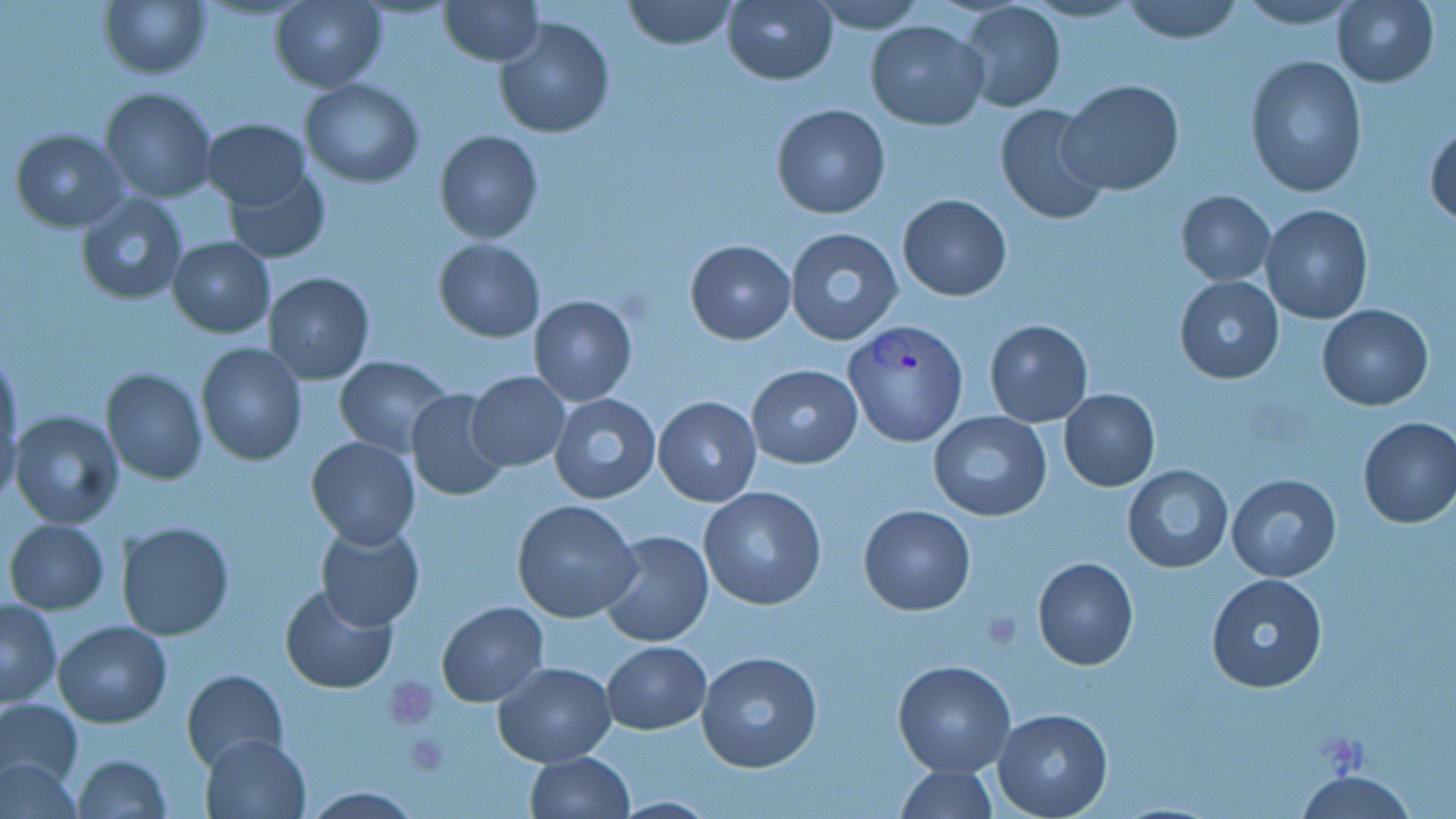

{
  "slide_level_diagnosis": "Plasmodium vivax",
  "preparation": "thin blood smear",
  "uninfected_red_blood_cell_locations": "approximate bounding boxes as [x1, y1, x2, y2] in pixels: [99, 0, 210, 79], [268, 0, 387, 91], [440, 0, 543, 66], [621, 0, 739, 50], [721, 0, 839, 85], [809, 0, 925, 31], [1121, 0, 1243, 44], [1234, 0, 1365, 28], [1333, 0, 1440, 86], [957, 2, 1066, 113], [494, 18, 616, 137], [865, 20, 988, 130], [1245, 55, 1365, 198], [301, 78, 423, 187], [1058, 80, 1185, 197], [99, 87, 217, 203], [993, 102, 1111, 225], [772, 103, 892, 220], [201, 118, 313, 210], [1426, 119, 1456, 228], [10, 128, 126, 231], [433, 130, 543, 243], [223, 167, 330, 263], [1176, 190, 1275, 286], [76, 194, 189, 306], [897, 194, 1012, 300], [1260, 205, 1374, 325], [785, 229, 904, 345], [168, 237, 275, 337], [433, 237, 545, 342], [685, 239, 794, 344], [262, 272, 375, 385], [1174, 274, 1283, 384], [529, 295, 637, 406], [1318, 304, 1434, 410], [984, 320, 1092, 426], [195, 342, 308, 466], [0, 351, 22, 480], [334, 356, 453, 457], [746, 363, 863, 470], [101, 368, 207, 484], [468, 371, 569, 472], [405, 388, 510, 501], [1058, 389, 1160, 491], [549, 393, 661, 503], [652, 395, 763, 507], [8, 411, 123, 530], [929, 413, 1052, 521], [1356, 416, 1456, 529], [306, 438, 420, 550], [1122, 464, 1232, 575], [1225, 472, 1342, 581], [699, 486, 827, 611], [512, 498, 641, 624], [859, 505, 975, 615], [4, 519, 110, 615], [117, 521, 233, 640], [315, 522, 424, 632], [598, 529, 714, 648], [1032, 557, 1139, 670], [1208, 574, 1327, 693], [279, 583, 399, 694], [0, 599, 61, 707], [437, 601, 549, 706], [53, 620, 172, 728], [601, 640, 711, 735], [696, 650, 823, 775], [893, 660, 1016, 777], [491, 661, 618, 765], [181, 668, 288, 769], [0, 697, 83, 792], [992, 709, 1112, 818], [200, 730, 313, 819], [524, 751, 636, 818], [71, 753, 172, 819], [0, 757, 82, 817], [895, 764, 999, 819], [1293, 770, 1421, 818]",
  "stain": "May-Grünwald-Giemsa",
  "field_of_view": "one of a larger specimen",
  "modality": "optical microscopy",
  "magnification": "1000x",
  "image_size": "1456×819 pixels",
  "plasmodium_vivax_infected_red_blood_cell_locations": "approximate bounding boxes as [x1, y1, x2, y2] in pixels: [843, 318, 968, 447]",
  "platelet_locations": "approximate bounding boxes as [x1, y1, x2, y2] in pixels: [384, 675, 439, 728], [400, 733, 452, 776]"
}